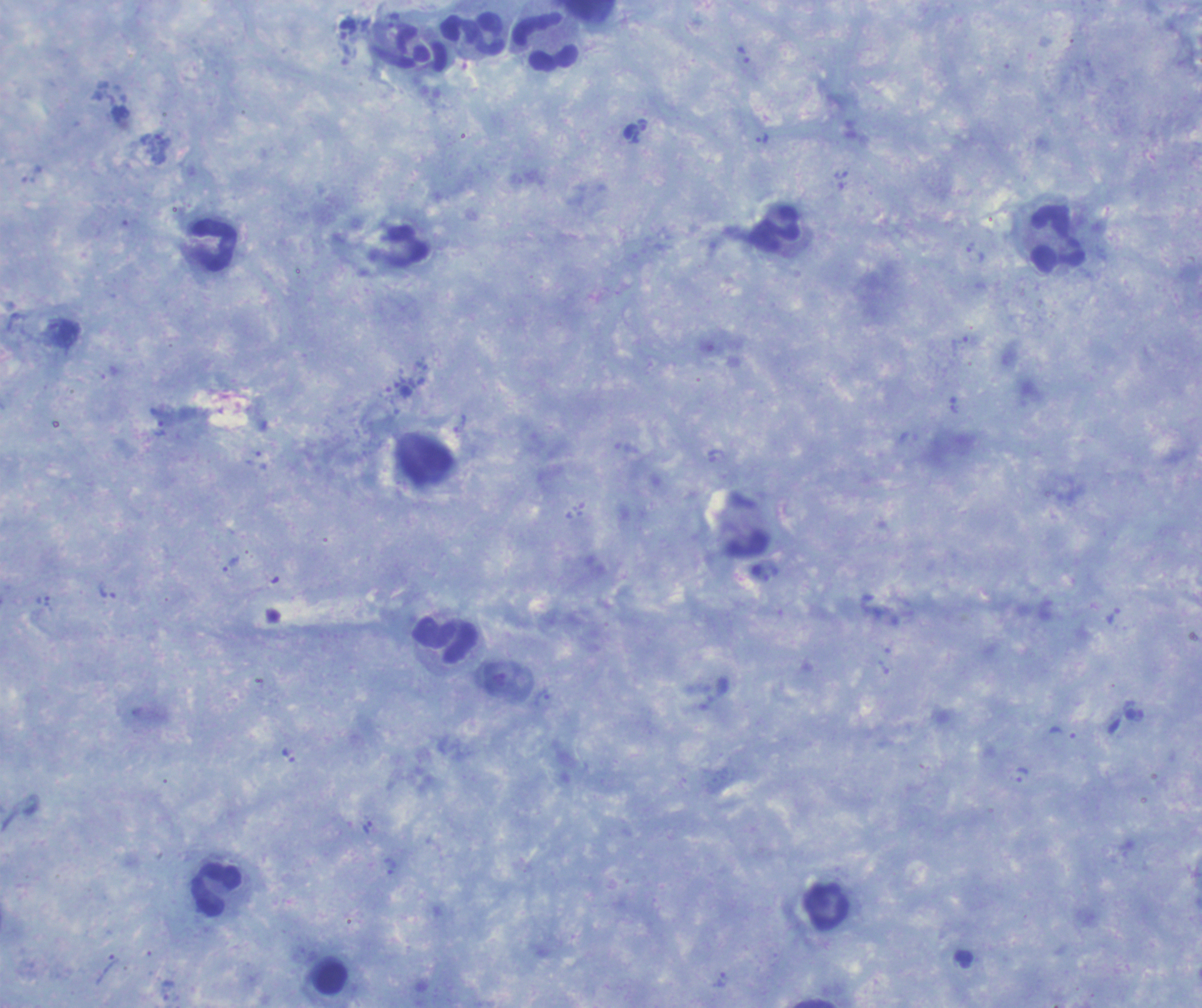 Approximate object centers, in pixels from the top-left corner. Leukocyte locations: (x=472, y=35), (x=545, y=43), (x=775, y=230), (x=1057, y=239), (x=213, y=245), (x=446, y=640), (x=216, y=890), (x=826, y=906), (x=330, y=979). Trophozoite locations: (x=640, y=134), (x=762, y=137), (x=975, y=254), (x=459, y=424), (x=232, y=564), (x=542, y=697), (x=1021, y=776), (x=390, y=867), (x=723, y=980). Image is 1202×1008 pixels. Coloration quality: good. Background quality: satisfactory. Captured at 100x magnification. Thick smear of blood. Result: Plasmodium parasites identified. Romanowsky stain. Previously used in a real diagnosis. Single field of view.